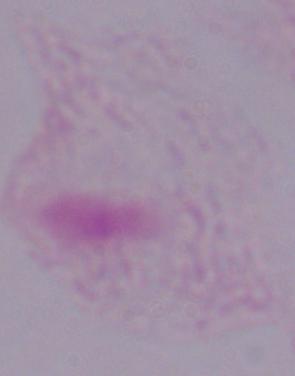
{
  "modality": "micrograph",
  "magnification": "1000x",
  "identification": "trichomonad"
}